Give the extent of all uninfected red blood cells.
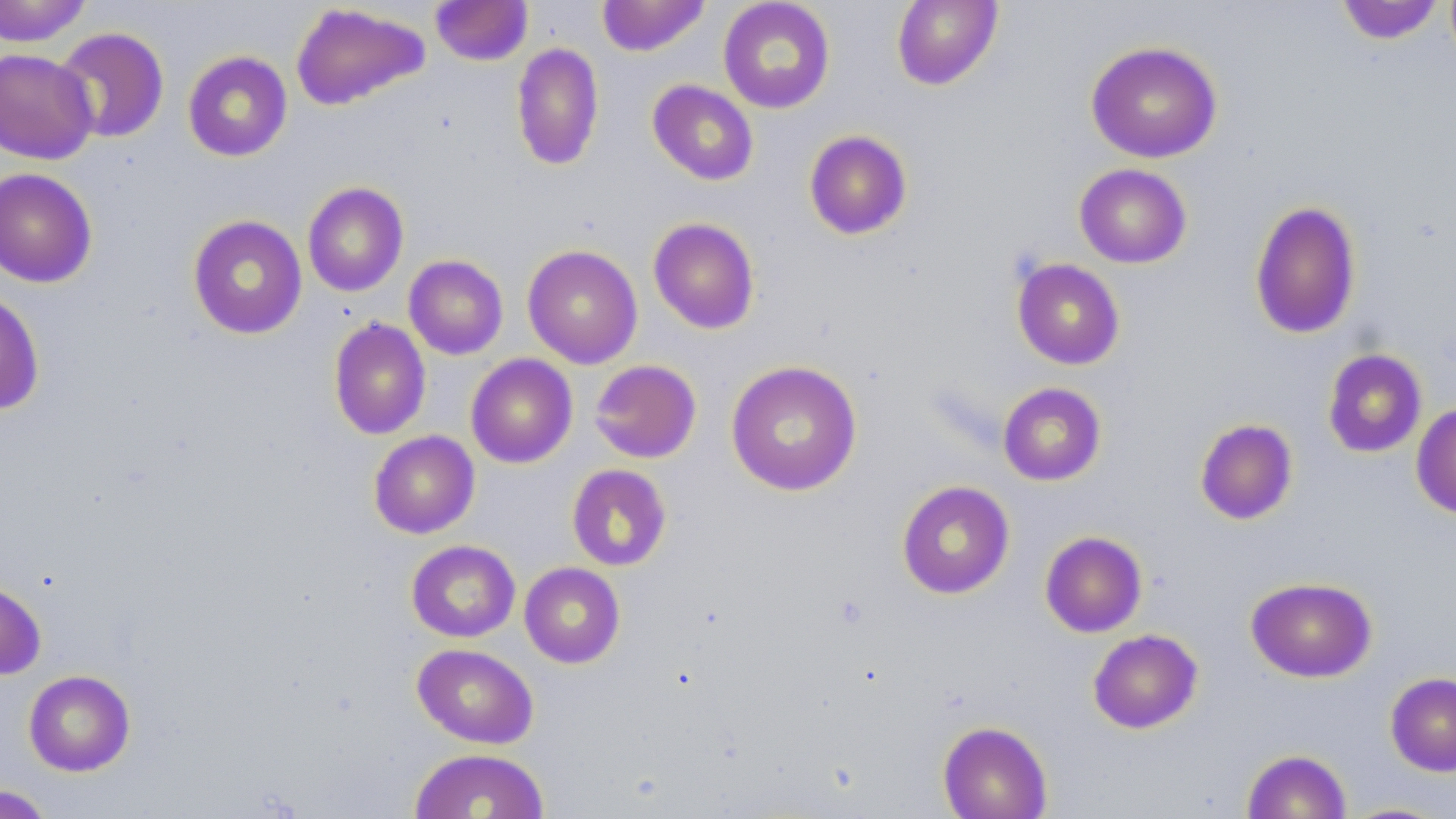
Approximate bounding boxes as (x1, y1, x2, y2) in pixels.
Uninfected red blood cells: (0, 0, 94, 46), (430, 0, 533, 66), (596, 0, 711, 56), (717, 0, 836, 114), (891, 0, 1004, 90), (1335, 1, 1447, 45), (290, 3, 430, 111), (53, 27, 170, 144), (1085, 40, 1223, 163), (510, 42, 604, 171), (0, 48, 98, 164), (182, 51, 293, 162), (647, 79, 759, 185), (803, 129, 913, 240), (1074, 163, 1192, 268), (0, 168, 99, 288), (302, 182, 409, 297), (1249, 200, 1362, 339), (187, 214, 308, 339), (648, 217, 760, 334), (522, 244, 643, 369), (404, 255, 508, 360), (1011, 258, 1126, 370), (0, 290, 46, 415), (328, 318, 431, 440), (1322, 348, 1427, 458), (465, 353, 578, 468), (589, 359, 702, 463), (725, 360, 863, 497), (998, 382, 1106, 486), (1411, 403, 1456, 520), (1194, 418, 1298, 525), (368, 430, 480, 539), (567, 464, 672, 571), (896, 480, 1015, 599), (1039, 531, 1148, 637), (406, 540, 520, 642), (519, 562, 625, 668), (1246, 576, 1377, 683), (0, 579, 47, 679), (1087, 629, 1203, 734), (412, 643, 539, 749), (23, 669, 135, 776), (1385, 672, 1456, 776), (937, 720, 1052, 819), (408, 748, 549, 819), (1241, 749, 1352, 819), (0, 785, 55, 818), (1337, 801, 1451, 818).

Slide-level diagnosis: no evidence of blood parasites. May-Grünwald-Giemsa stain. Thin blood film. Single field of view. Optical microscopy. Image is 1456×819 pixels. Captured at 1000x magnification.